Assess this cell for malaria.
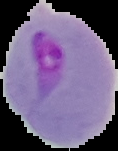
Parasitized.

From a thin blood film. The area outside the segmented cell region is set to black. Image is 118×151 pixels.